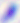

Toxoplasma gondii is seen. 400x magnification. Photomicrograph.